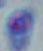
Photomicrograph. 1000x magnification. Toxoplasma gondii is seen.